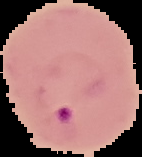

Summary:
  - Malaria status: parasitized
  - Image size: 142×157 pixels
  - Image type: segmented cell region on a black background
  - Preparation: thin blood smear